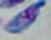
Summary:
  - Modality: photomicrograph
  - Identification: Toxoplasma gondii
  - Magnification: 1000x